Name the cell type shown.
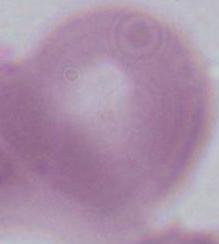

An erythrocyte.

{
  "modality": "micrograph",
  "magnification": "1000x"
}